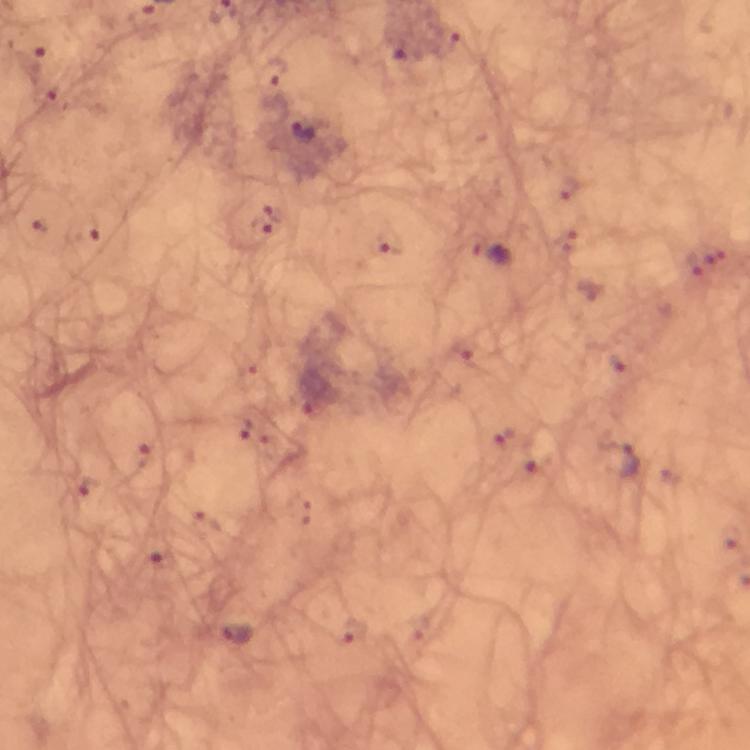 Approximate object centers, in pixels from the top-left corner. Malaria parasite locations: (x=30, y=64), (x=47, y=96), (x=305, y=133), (x=260, y=226), (x=388, y=241), (x=490, y=254), (x=310, y=394), (x=621, y=462), (x=235, y=635). Giemsa stain. Immersion oil was used. Thick blood smear. From a diagnostic examination for malaria. Image is 750×750 pixels. 100x magnification. A crop from one field of view. Photographed with a smartphone mounted on the microscope.